Give the position of every Plasmodium parasite visible.
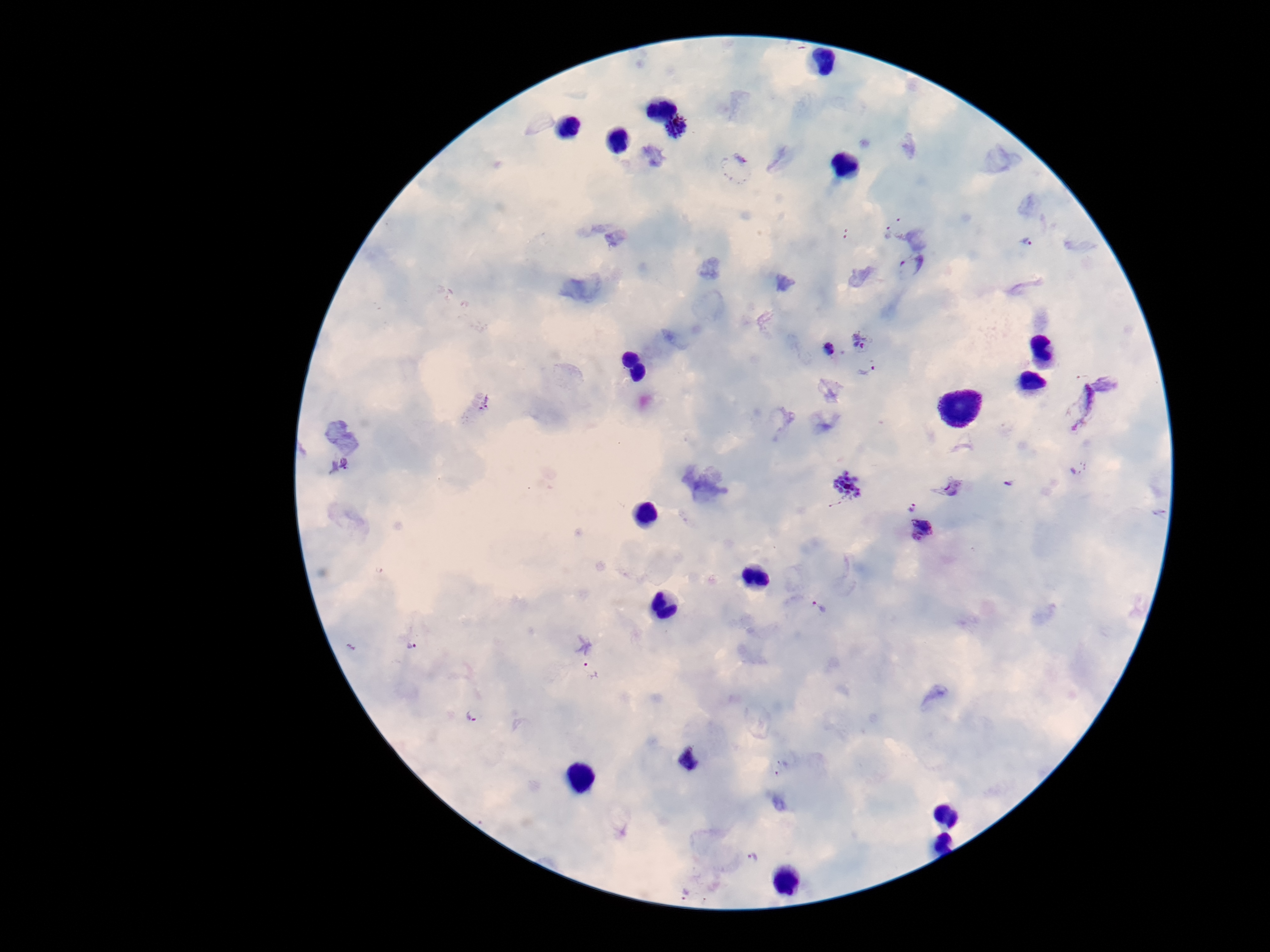

Approximate centers as (x, y) in pixels.
Plasmodium parasites: (679, 130), (888, 232), (1028, 241), (912, 265), (864, 340), (827, 349), (867, 370), (1109, 381), (481, 401), (1073, 405), (338, 465), (1078, 467), (949, 484), (1009, 484), (848, 486), (834, 504), (912, 506), (921, 530), (819, 607), (409, 644), (590, 671), (473, 714), (688, 759), (781, 767), (751, 858), (685, 893).

patient malaria status = positive
field of view = one from this slide
capture = smartphone camera through the microscope eyepiece
preparation = thick blood film
magnification = 100x
stain = Giemsa
image size = 1270×952 pixels